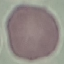

Result: no malaria parasites detected. Thin blood film. Cell patch, automatically extracted from a larger field of view and resized to 64 × 64 pixels. Giemsa-stained preparation. Acquired by smartphone through the microscope eyepiece.